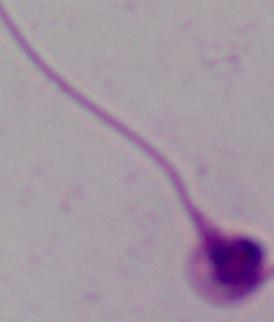
Summary:
  - Modality: micrograph
  - Identification: Leishmania
  - Magnification: 1000x